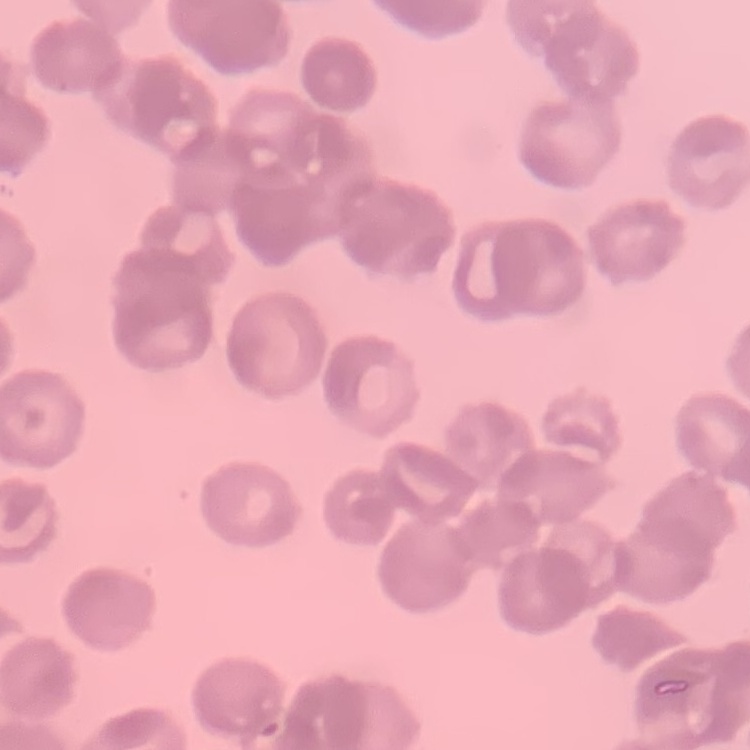

The erythrocytes exhibit rouleaux formation. One tile cut from a larger photomicrograph. Field's or Giemsa stain. Thin blood smear.